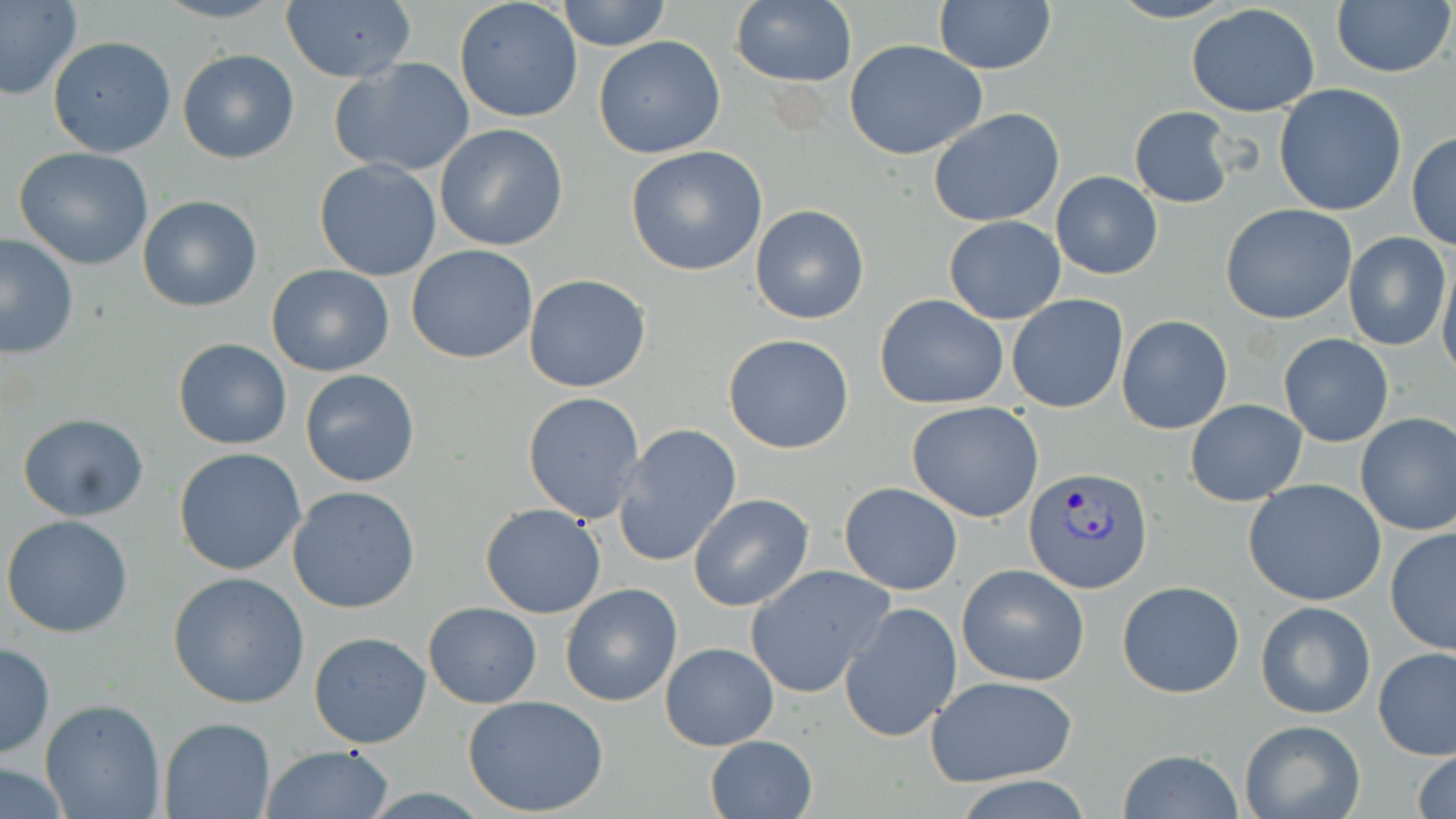 Approximate bounding boxes as (x1,y1)-(x2,y2) corner pairs in pixels. Plasmodium vivax-infected red blood cell locations: (1023,466)-(1154,595). Uninfected red blood cell locations: (0,0)-(82,101), (153,0)-(285,24), (559,0)-(670,50), (731,0)-(856,87), (934,0)-(1056,75), (1107,0)-(1235,24), (1330,0)-(1454,80), (280,2)-(417,83), (454,2)-(583,121), (1186,2)-(1321,118), (47,35)-(177,158), (594,35)-(726,159), (845,39)-(987,159), (178,48)-(300,164), (330,56)-(475,176), (1273,83)-(1408,216), (1130,106)-(1235,207), (928,107)-(1065,227), (435,123)-(568,251), (1406,131)-(1456,251), (624,146)-(768,276), (13,147)-(154,269), (313,160)-(442,282), (1051,172)-(1162,279), (139,195)-(261,312), (1220,203)-(1358,324), (750,205)-(870,325), (944,216)-(1066,324), (0,232)-(79,360), (1345,232)-(1451,350), (406,244)-(539,364), (1439,257)-(1456,384), (265,264)-(395,378), (523,273)-(652,392), (875,294)-(1009,408), (1006,295)-(1128,412), (1117,314)-(1232,434), (722,334)-(855,454), (1278,334)-(1395,448), (172,338)-(293,450), (298,369)-(420,489), (522,390)-(647,525), (1185,398)-(1307,505), (907,401)-(1045,522), (1354,411)-(1456,535), (17,414)-(150,523), (611,424)-(742,568), (174,446)-(307,577), (1243,478)-(1390,607), (839,482)-(964,596), (287,486)-(420,614), (688,493)-(815,613), (480,502)-(607,618), (2,516)-(134,638), (1384,526)-(1456,656), (956,563)-(1090,686), (746,564)-(894,697), (168,572)-(310,709), (1117,580)-(1245,699), (560,583)-(683,706), (1255,600)-(1376,719), (424,601)-(541,708), (838,601)-(962,744), (309,631)-(432,749), (0,641)-(55,761), (660,642)-(779,750), (1374,647)-(1455,761), (924,676)-(1079,787), (462,694)-(608,817), (39,699)-(166,819), (159,717)-(274,819), (1238,719)-(1365,819), (705,735)-(816,819), (258,744)-(396,819), (1413,748)-(1456,819), (1118,749)-(1244,819), (1,765)-(71,816), (957,774)-(1094,819). Slide-level diagnosis: Plasmodium vivax. Captured at 1000x magnification. One field of a larger specimen. Thin blood film. May-Grünwald-Giemsa-stained preparation. Optical microscopy. Image is 1456×819 pixels.